Give the position of every Plasmodium parasite.
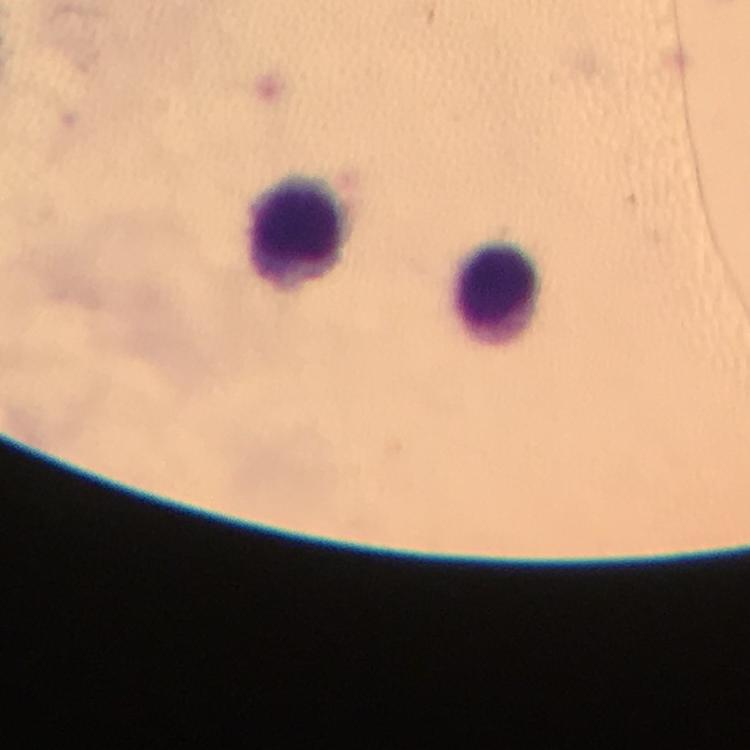
No Plasmodium parasites detected.

Approximate centers as [x, y] in pixels. Leukocyte locations: [297, 230], [500, 294]. 100x magnification. Smartphone photograph taken through a microscope. A crop from one field of view. Thick smear. From a malaria diagnostic workup. Image is 750×750 pixels. Giemsa stain. Immersion oil was used.